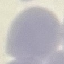
{
  "result": "no malaria parasites detected",
  "preparation": "thin blood film",
  "stain": "Giemsa",
  "image_type": "automatically extracted cell patch, resized to 64 × 64 pixels",
  "capture": "smartphone through the microscope eyepiece"
}